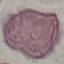
Malaria status: uninfected. Acquired by smartphone through the microscope eyepiece. Thin blood film. Cell patch, automatically extracted from a larger field of view and resized to 64 × 64 pixels. Giemsa stain.